State which parasite is depicted.
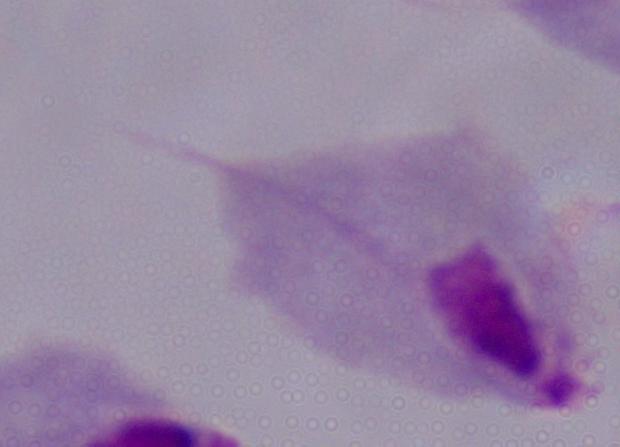
A trichomonad.

Summary:
  - Modality: photomicrograph
  - Magnification: 1000x